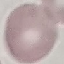 Result: no malaria parasites seen. Giemsa-stained preparation. Thin blood film. Cell patch, automatically extracted from a larger field of view and resized to 64 × 64 pixels. Photographed with a smartphone camera at the microscope eyepiece.